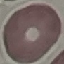
result = no malaria parasites detected
capture = smartphone camera at the microscope eyepiece
image type = cell patch, automatically extracted from a larger field of view and resized to 64 × 64 pixels
stain = Giemsa
preparation = thin smear